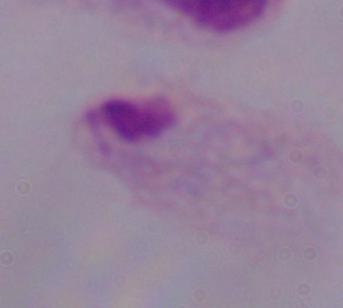 1000x magnification. Photomicrograph. A trichomonad is seen.